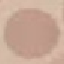
malaria status = uninfected
stain = Giemsa
capture = smartphone through the microscope eyepiece
image type = cell patch, automatically extracted from a larger field of view and resized to 64 × 64 pixels
preparation = thin blood smear